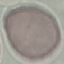
Malaria status: uninfected. Thin blood film. Acquired by smartphone through the microscope eyepiece. Cell patch, automatically extracted from a larger field of view and resized to 64 × 64 pixels. Giemsa-stained preparation.